Report the malaria status of this cell.
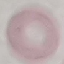
Uninfected.

{
  "stain": "Giemsa",
  "capture": "smartphone through the microscope eyepiece",
  "preparation": "thin blood film",
  "image_type": "automatically extracted cell patch, resized to 64 × 64 pixels"
}